Give the position of every Plasmodium parasite visible.
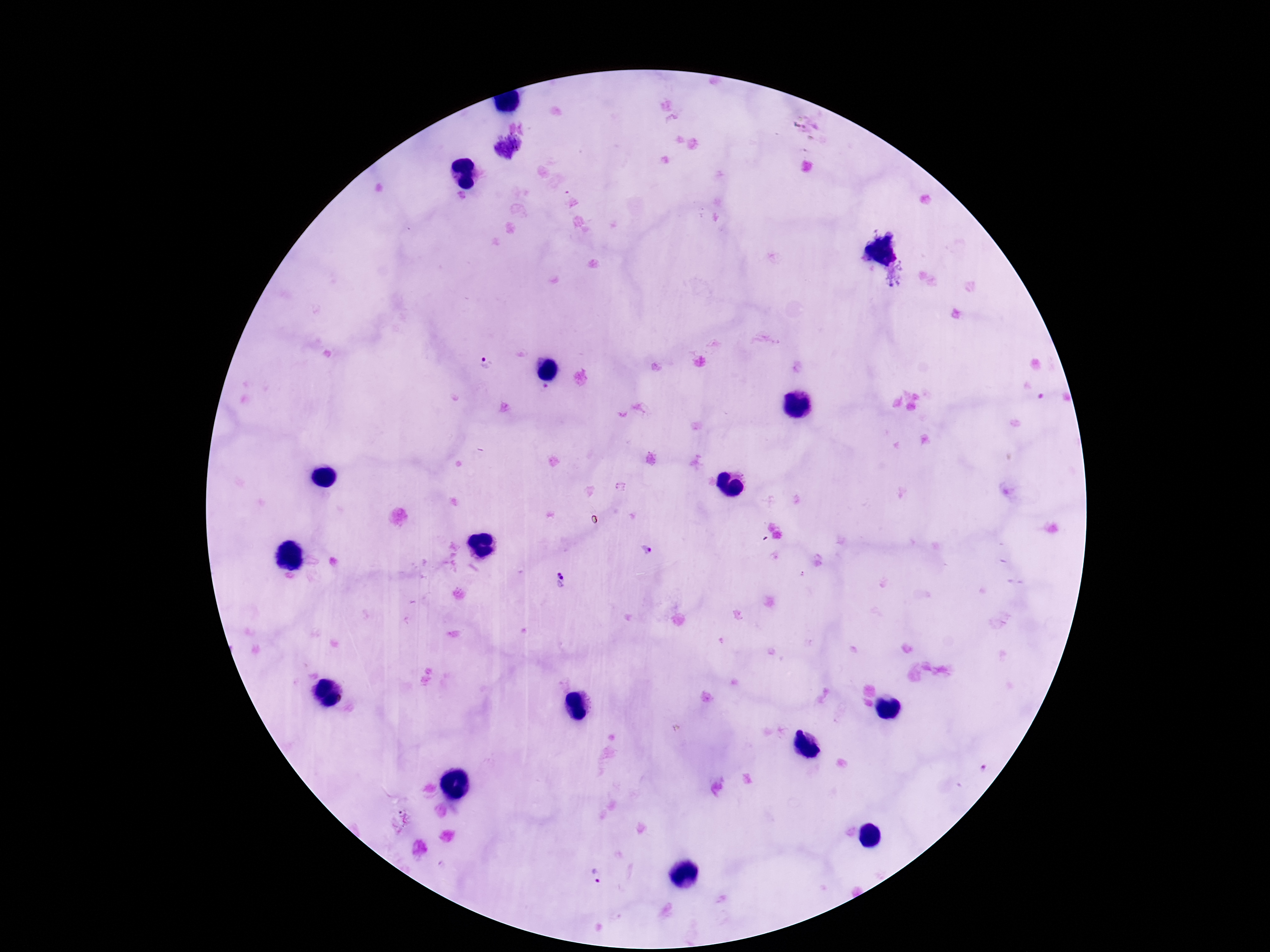
Approximate centers as [x, y] in pixels.
Plasmodium parasites: [516, 139], [502, 149], [485, 363], [646, 549], [561, 575], [596, 878].

Summary:
  - Capture: smartphone camera through the microscope eyepiece
  - Preparation: thick blood smear
  - Image size: 1270×952 pixels
  - Magnification: 100x
  - Field of view: single
  - Stain: Giemsa
  - Patient malaria status: infected